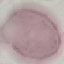
Summary:
  - Result: negative for malaria parasites
  - Image type: automatically extracted cell patch, resized to 64 × 64 pixels
  - Preparation: thin smear
  - Stain: Giemsa
  - Capture: smartphone through the microscope eyepiece